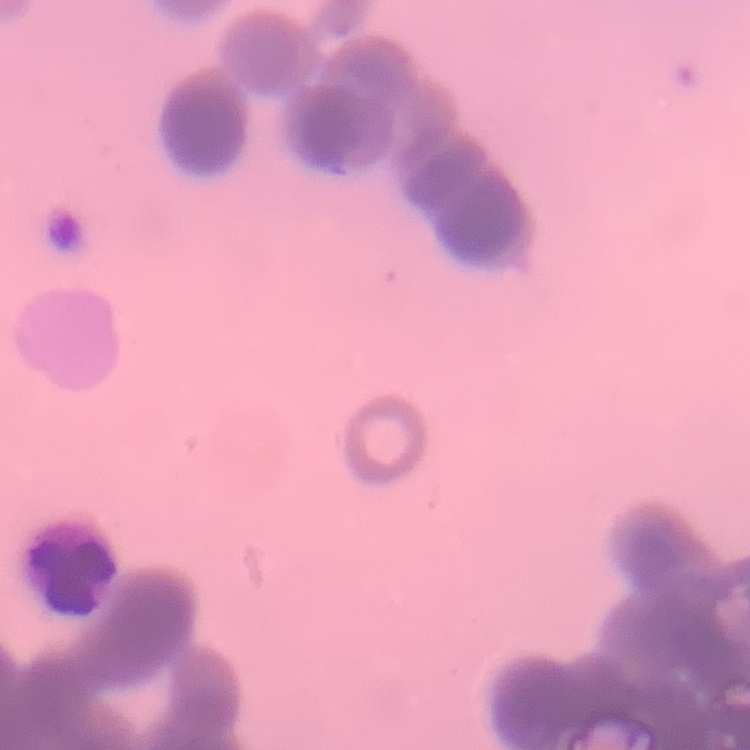

The red blood cells show rouleaux formation. Thin blood smear. One tile cut from a larger photomicrograph. Field's or Giemsa stain.